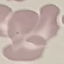

Malaria status: uninfected. Automatically extracted cell patch, resized to 64 × 64 pixels. Thin smear of blood. Giemsa stain. Acquired by smartphone through the microscope eyepiece.